Comment on the morphology of the red blood cells.
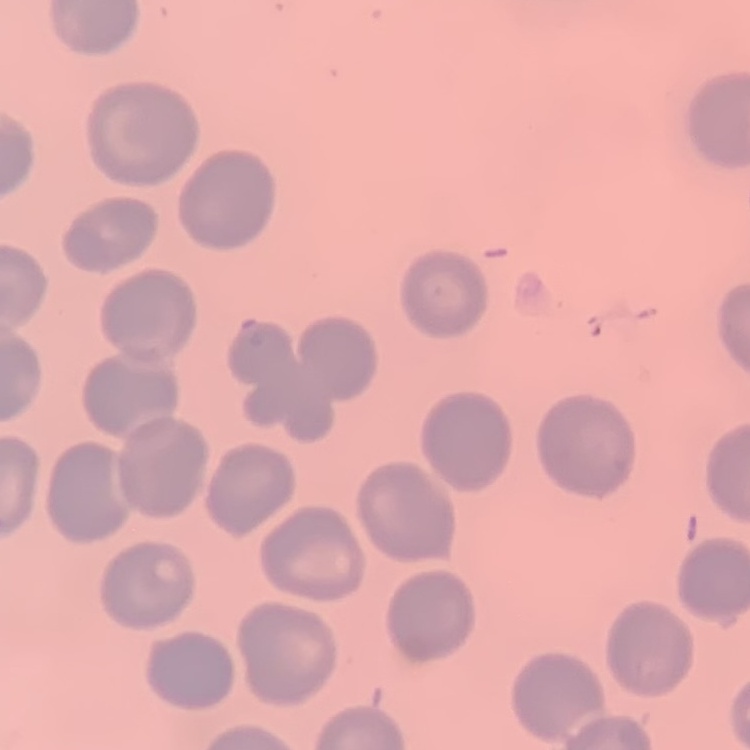

They show no rouleaux formation.

Square crop of a larger photomicrograph. Thin blood film. Stained with either Field's or Giemsa.